Comment on the morphology of the erythrocytes.
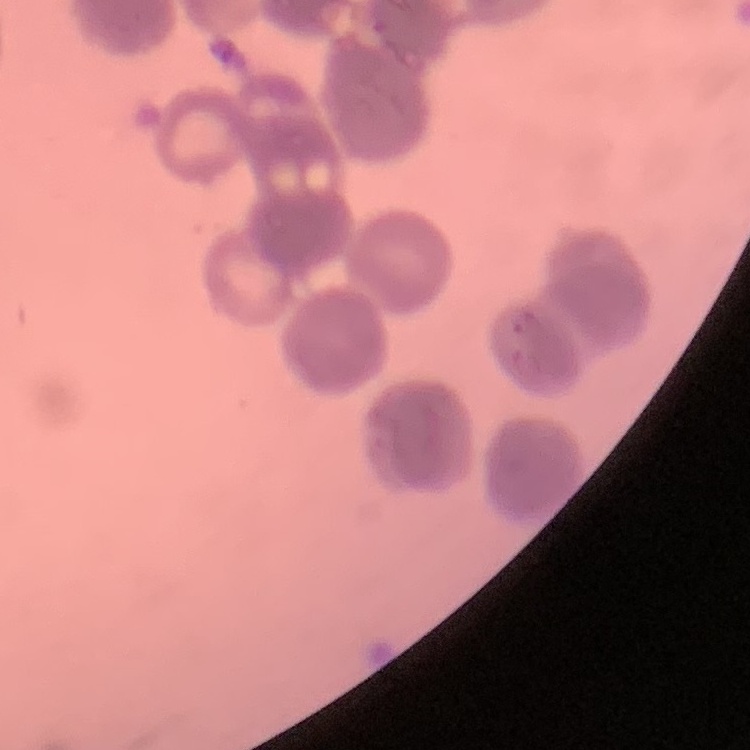

Rouleaux formation.

Thin blood film. One tile cut from a larger photomicrograph. Field's or Giemsa stain.